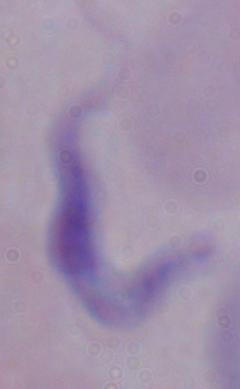

Summary:
  - Modality: micrograph
  - Magnification: 1000x
  - Identification: trypanosome